Look for parasitized red blood cells.
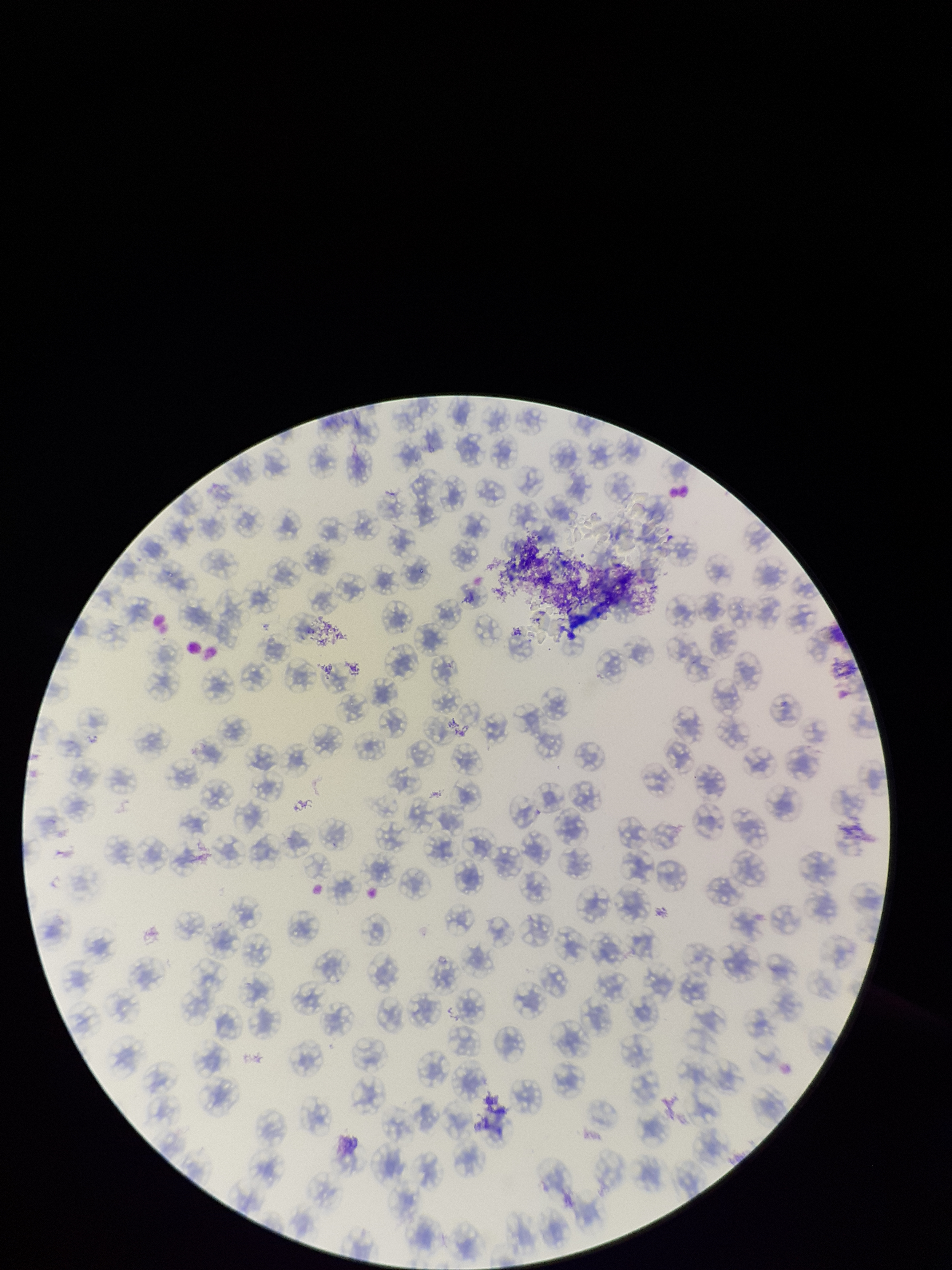

None identified.

Image is 952×1270 pixels. Patient malaria status: negative. Single field of view. Red blood cell count: 115. Giemsa stain. Parasitized red blood cell count: 0. Preparation: thin. Smartphone photograph taken through the eyepiece of a microscope.